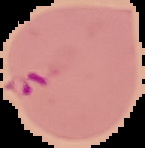
image type = segmented cell region on a black background
image size = 145×148 pixels
malaria status = parasitized
preparation = thin blood film